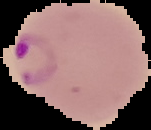 Malaria status: parasitized. Image is 151×130 pixels. From a thin blood film. Cell region segmented out of the field of view; the surrounding area is masked to black.